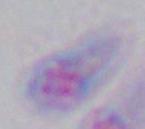 Micrograph. 1000x magnification. Toxoplasma gondii is shown.